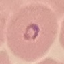
Summary:
  - Result: malaria parasites detected
  - Stain: Giemsa
  - Capture: smartphone camera at the microscope eyepiece
  - Preparation: thin blood film
  - Image type: automatically extracted cell patch, resized to 64 × 64 pixels